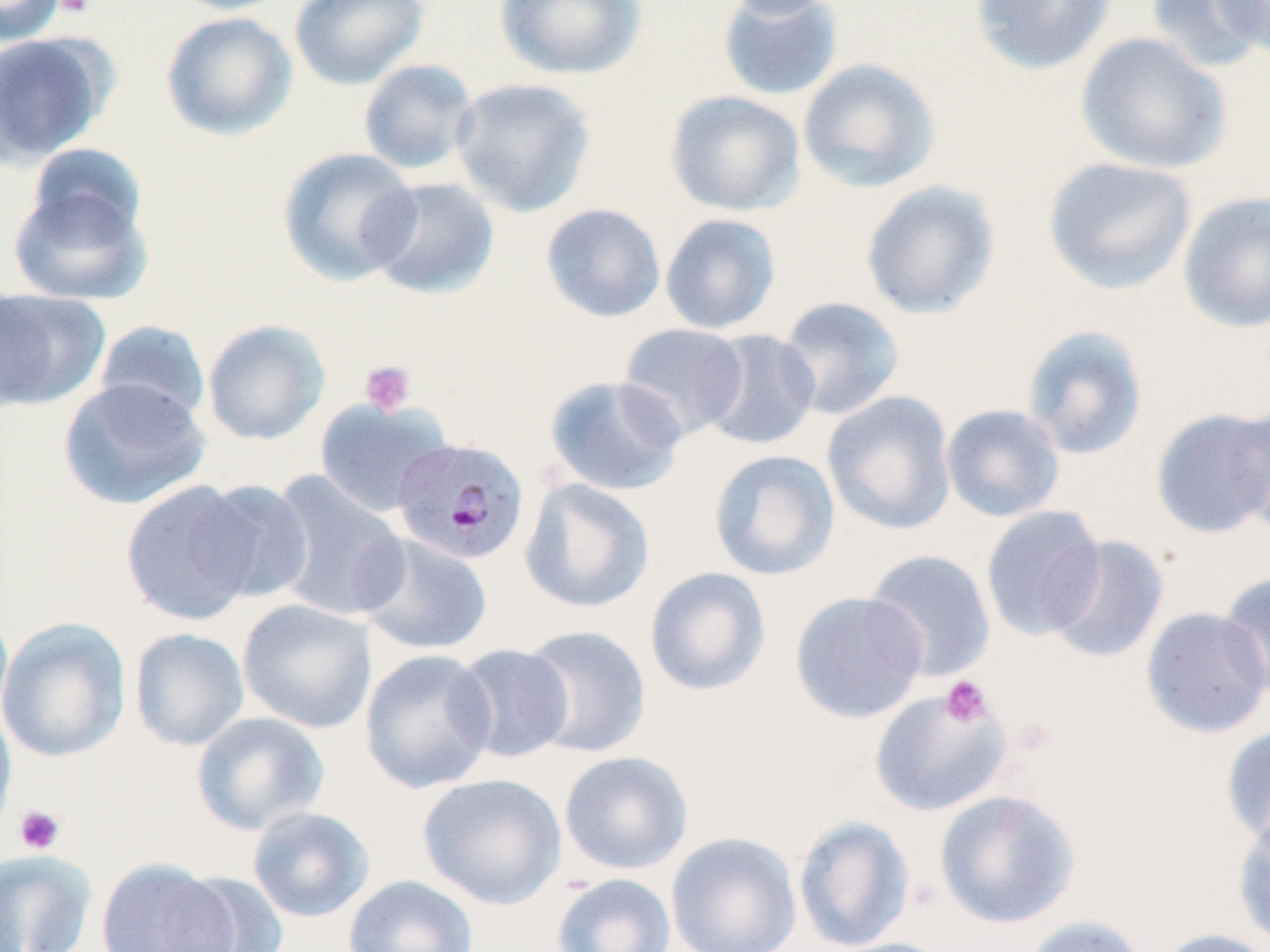

Approximate bounding boxes as (x1, y1, x2, y2) in pixels. Platelet locations: (54, 0, 93, 17), (359, 360, 416, 416), (940, 676, 994, 729), (1008, 716, 1058, 759), (13, 805, 65, 855). Uninfected red blood cell locations: (0, 0, 67, 46), (165, 0, 296, 16), (289, 0, 430, 91), (494, 0, 647, 80), (717, 0, 844, 101), (720, 0, 844, 20), (970, 0, 1115, 75), (1145, 0, 1269, 74), (1212, 0, 1270, 58), (160, 11, 297, 140), (0, 31, 112, 169), (1074, 31, 1231, 175), (797, 58, 940, 194), (358, 59, 478, 175), (450, 77, 596, 217), (664, 90, 805, 217), (26, 143, 148, 244), (276, 147, 422, 286), (1042, 156, 1197, 295), (364, 177, 500, 300), (860, 180, 1000, 319), (7, 182, 152, 305), (1177, 190, 1270, 333), (540, 203, 666, 322), (660, 213, 781, 335), (0, 287, 111, 411), (776, 295, 905, 421), (94, 320, 211, 423), (202, 320, 330, 445), (618, 323, 749, 441), (1020, 324, 1149, 461), (699, 329, 821, 450), (544, 374, 686, 497), (59, 377, 211, 510), (822, 391, 957, 536), (314, 398, 452, 517), (1227, 401, 1270, 538), (940, 403, 1066, 523), (1149, 406, 1270, 539), (708, 449, 840, 580), (267, 472, 409, 622), (121, 478, 264, 625), (518, 478, 655, 613), (193, 480, 314, 604), (980, 505, 1107, 641), (355, 533, 493, 656), (1045, 534, 1170, 664), (864, 549, 996, 682), (644, 566, 771, 697), (1218, 571, 1270, 700), (789, 590, 929, 723), (237, 599, 377, 734), (0, 600, 14, 734), (1139, 606, 1270, 740), (0, 616, 131, 763), (519, 624, 652, 758), (129, 627, 249, 751), (451, 643, 575, 763), (358, 648, 498, 794), (869, 688, 1012, 817), (0, 704, 17, 840), (191, 711, 329, 836), (1220, 724, 1270, 849), (559, 750, 693, 874), (417, 773, 566, 909), (934, 789, 1080, 929), (247, 805, 375, 922), (1232, 811, 1270, 947), (793, 815, 915, 952), (666, 832, 802, 952), (0, 848, 97, 952), (95, 859, 237, 952), (551, 872, 677, 952), (172, 873, 289, 951), (343, 875, 478, 952), (1022, 914, 1150, 952), (1151, 928, 1270, 952), (818, 937, 957, 952). Plasmodium malariae-infected red blood cell locations: (391, 437, 530, 565). Slide-level diagnosis: Plasmodium malariae. May-Grünwald-Giemsa stain. One field of a larger specimen. Image is 1270×952 pixels. Thin blood smear. Optical microscopy. Captured at 1000x magnification.